Classify this cell by malaria status.
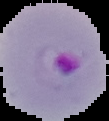
It is parasitized.

From a thin blood smear. Cell region segmented out of the field of view; the surrounding area is masked to black. Image is 109×121 pixels.